Locate every P. falciparum parasite and identify its life-cycle stage.
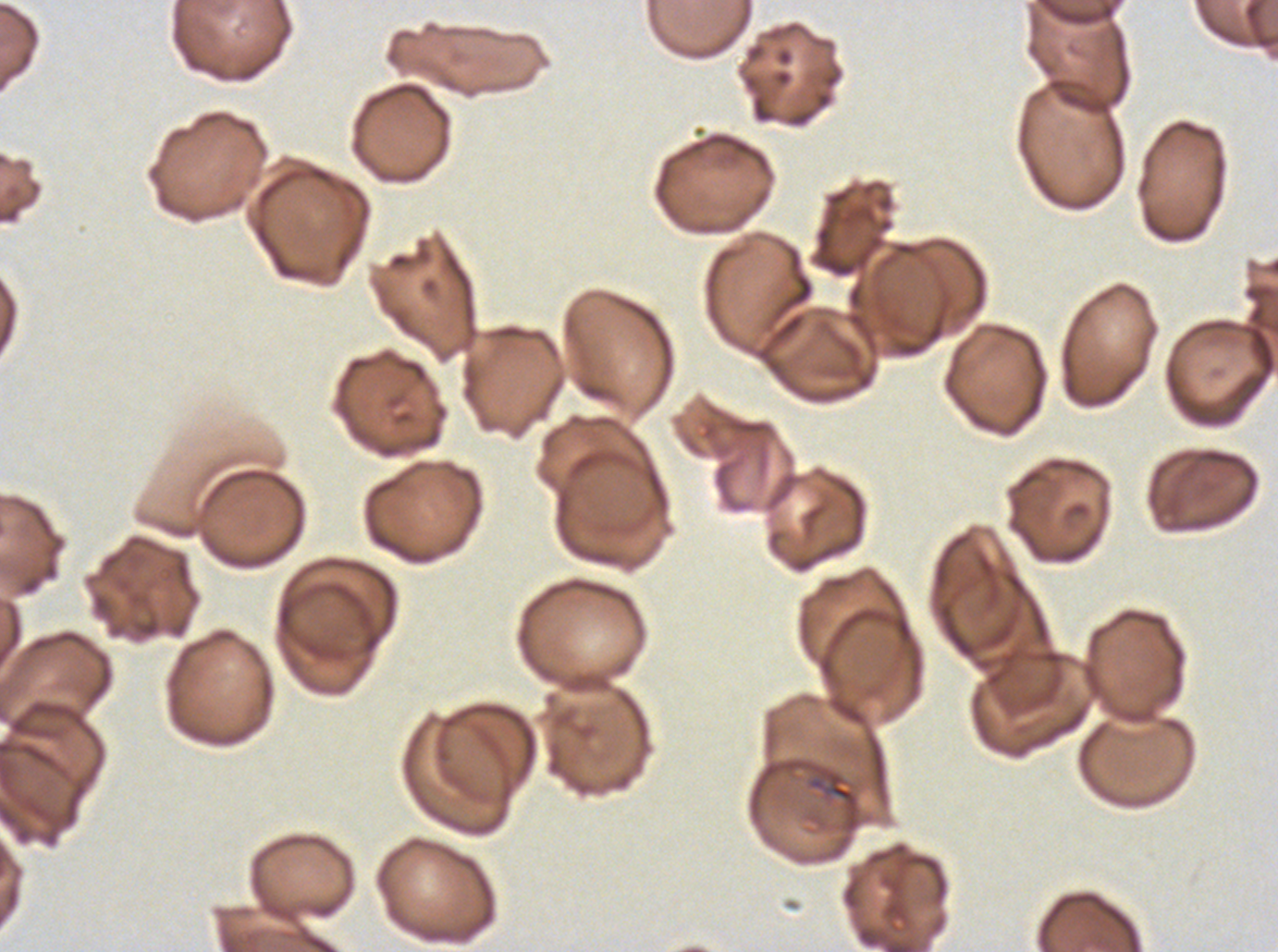

No rings, late-ring/early-trophozoite forms, mid trophozoites, late trophozoites, early schizonts, late schizonts, segmenters, or gametocytes observed.

preparation: thin blood smear
stain: Giemsa
debris_locations: 'approximate bounding boxes as {x1, y1, x2, y2} in pixels: {829, 783, 854, 802}'
specimen: P. falciparum from a patient in The Gambia, cultured ex vivo for 24 to 48 hours
field_of_view: sub-image separated from a larger composite
image_size: 1278×952 pixels